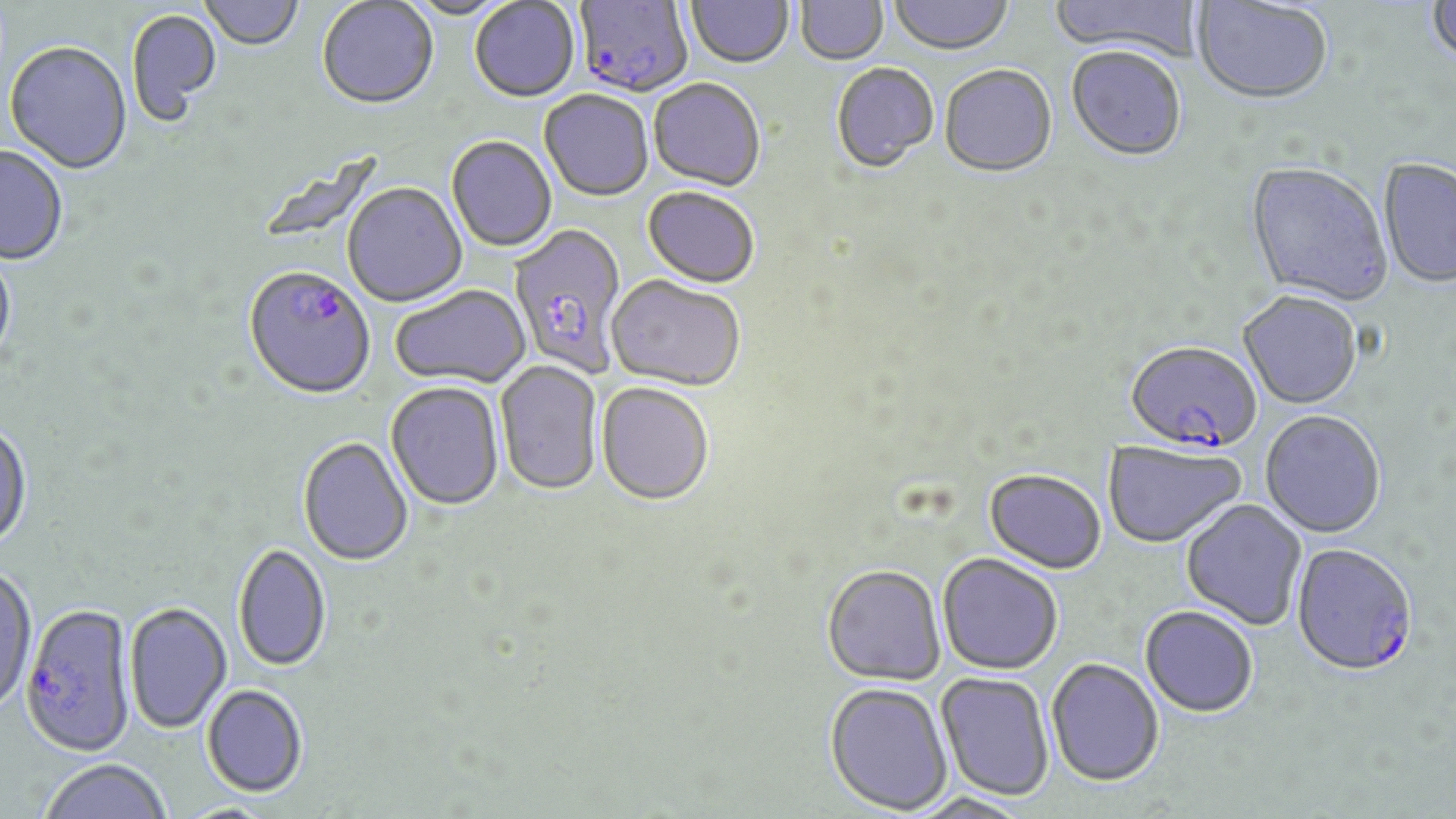
Summary:
  - Coordinate format: approximate bounding boxes as named x1/y1/x2/y2 corners in pixels
  - Plasmodium falciparum-infected red blood cell locations: (x1=575, y1=1, x2=692, y2=100), (x1=507, y1=225, x2=629, y2=378), (x1=243, y1=269, x2=376, y2=403), (x1=1125, y1=343, x2=1261, y2=456), (x1=1290, y1=544, x2=1418, y2=681), (x1=20, y1=604, x2=137, y2=761)
  - Uninfected red blood cell locations: (x1=198, y1=0, x2=304, y2=52), (x1=404, y1=0, x2=514, y2=22), (x1=888, y1=0, x2=1013, y2=57), (x1=1049, y1=0, x2=1205, y2=62), (x1=1425, y1=0, x2=1456, y2=72), (x1=317, y1=1, x2=439, y2=113), (x1=470, y1=1, x2=580, y2=104), (x1=686, y1=1, x2=794, y2=71), (x1=795, y1=1, x2=888, y2=68), (x1=1191, y1=1, x2=1333, y2=107), (x1=127, y1=9, x2=223, y2=127), (x1=4, y1=43, x2=133, y2=176), (x1=1066, y1=49, x2=1187, y2=164), (x1=831, y1=64, x2=940, y2=175), (x1=940, y1=66, x2=1058, y2=180), (x1=649, y1=81, x2=765, y2=194), (x1=539, y1=92, x2=653, y2=203), (x1=446, y1=137, x2=556, y2=254), (x1=0, y1=146, x2=68, y2=267), (x1=1379, y1=160, x2=1456, y2=290), (x1=1245, y1=163, x2=1392, y2=309), (x1=343, y1=183, x2=468, y2=309), (x1=642, y1=188, x2=759, y2=290), (x1=0, y1=248, x2=16, y2=369), (x1=606, y1=276, x2=745, y2=395), (x1=390, y1=286, x2=531, y2=392), (x1=1238, y1=292, x2=1362, y2=411), (x1=495, y1=361, x2=603, y2=498), (x1=386, y1=383, x2=504, y2=512), (x1=596, y1=384, x2=715, y2=509), (x1=1260, y1=411, x2=1386, y2=539), (x1=0, y1=422, x2=32, y2=554), (x1=297, y1=438, x2=413, y2=568), (x1=1104, y1=442, x2=1245, y2=549), (x1=983, y1=471, x2=1106, y2=576), (x1=1181, y1=499, x2=1307, y2=631), (x1=233, y1=544, x2=331, y2=674), (x1=937, y1=555, x2=1063, y2=677), (x1=0, y1=566, x2=38, y2=716), (x1=822, y1=567, x2=947, y2=688), (x1=125, y1=603, x2=232, y2=735), (x1=1139, y1=607, x2=1258, y2=718), (x1=1046, y1=659, x2=1164, y2=789), (x1=936, y1=673, x2=1054, y2=802), (x1=824, y1=684, x2=953, y2=816), (x1=201, y1=687, x2=307, y2=800), (x1=40, y1=760, x2=171, y2=819)
  - Slide-level diagnosis: Plasmodium falciparum
  - Stain: May-Grünwald-Giemsa
  - Field of view: single
  - Image size: 1456×819 pixels
  - Preparation: thin blood smear
  - Magnification: 1000x
  - Modality: light microscopy